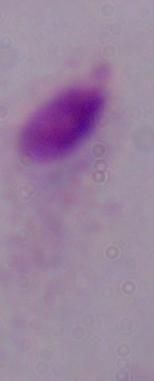
Summary:
  - Modality: micrograph
  - Identification: trichomonad
  - Magnification: 1000x